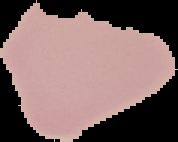

image_size: 178×142 pixels
malaria_status: uninfected
preparation: thin blood smear
image_type: segmented cell region with the area outside set to black